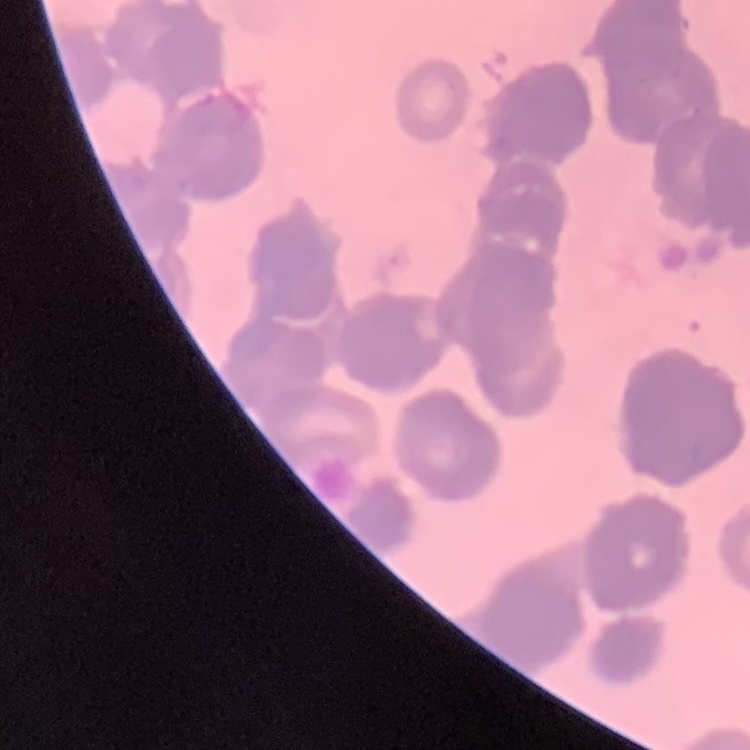

{
  "red_blood_cell_morphology": "rouleaux formation",
  "preparation": "thin blood smear",
  "image_type": "square crop of a larger photomicrograph",
  "stain": "Field's or Giemsa"
}